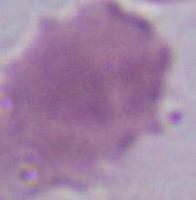
{
  "magnification": "1000x",
  "identification": "erythrocyte",
  "modality": "micrograph"
}